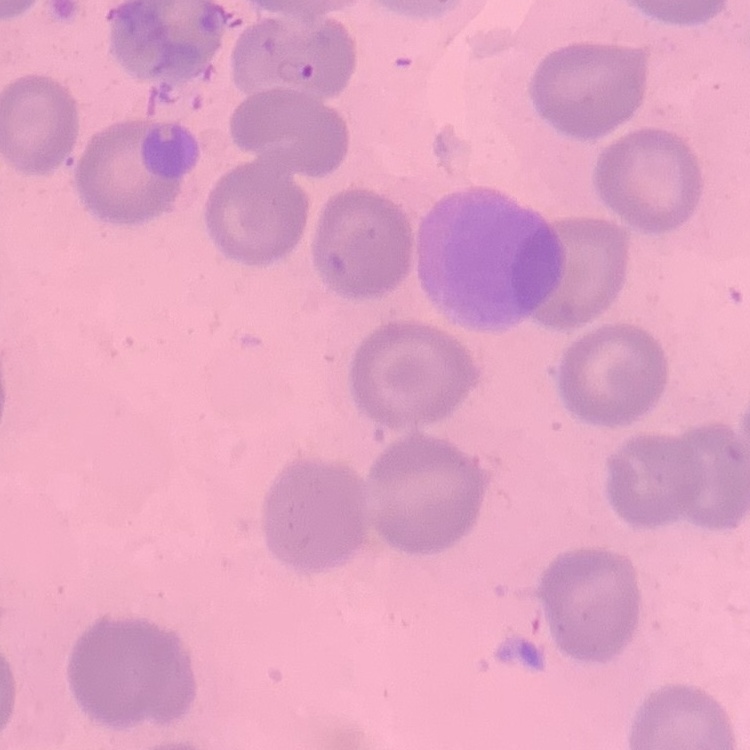
The erythrocytes exhibit no rouleaux formation. Stained with either Field's or Giemsa. Thin blood film. One tile cut from a larger photomicrograph.